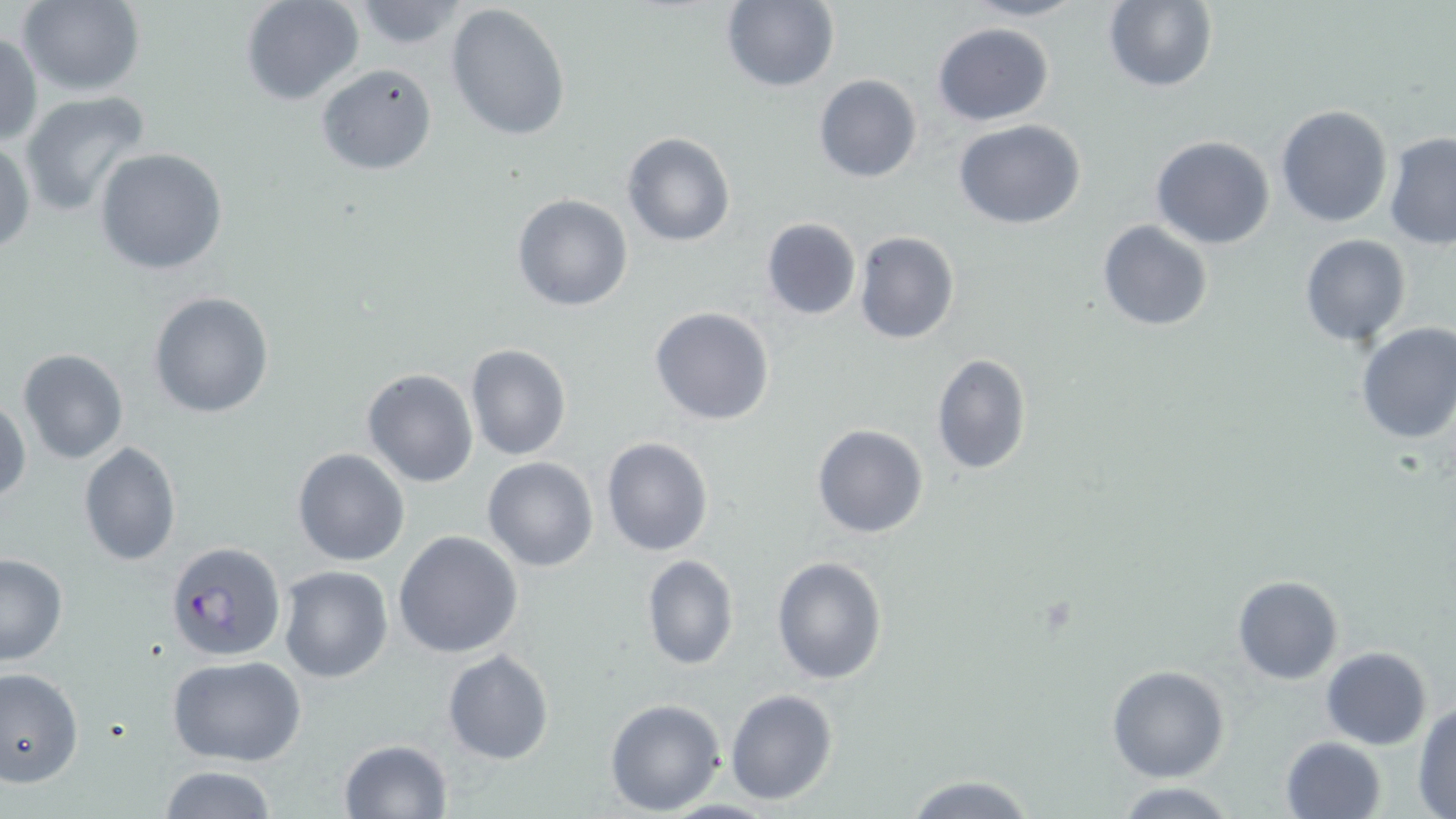
Summary:
  - Coordinate format: approximate bounding boxes as (x1,y1)-(x2,y2) corner pairs in pixels
  - Uninfected red blood cell locations: (240,0)-(364,106), (717,0)-(841,92), (964,0)-(1085,23), (16,1)-(147,96), (1102,1)-(1219,92), (349,2)-(471,52), (444,3)-(572,143), (932,21)-(1054,125), (0,32)-(42,147), (314,63)-(438,175), (812,73)-(923,183), (19,92)-(154,217), (1274,104)-(1394,228), (952,118)-(1087,230), (1382,129)-(1455,249), (622,132)-(735,247), (1150,135)-(1276,251), (0,139)-(36,257), (94,146)-(229,276), (511,193)-(633,313), (760,218)-(862,320), (1096,219)-(1213,333), (854,231)-(960,344), (1299,233)-(1411,347), (148,290)-(275,419), (649,306)-(777,425), (1354,321)-(1456,445), (466,344)-(571,460), (16,349)-(130,465), (930,353)-(1032,476), (361,367)-(479,488), (0,399)-(30,506), (811,423)-(928,539), (600,436)-(713,556), (78,442)-(182,566), (292,447)-(411,566), (482,457)-(598,572), (394,529)-(524,659), (0,554)-(69,667), (640,555)-(738,670), (771,555)-(888,685), (278,565)-(394,682), (1232,575)-(1344,684), (1321,647)-(1432,749), (442,649)-(555,764), (168,655)-(307,766), (0,665)-(84,789), (1107,665)-(1230,782), (725,688)-(840,805), (604,698)-(725,815), (1413,702)-(1456,816), (1279,736)-(1385,819), (338,739)-(452,818), (157,765)-(280,819), (902,774)-(1038,817), (1113,781)-(1242,817)
  - Plasmodium falciparum-infected red blood cell locations: (166,540)-(287,664)
  - Slide-level diagnosis: Plasmodium falciparum
  - Modality: light microscopy
  - Stain: May-Grünwald-Giemsa
  - Preparation: thin blood film
  - Magnification: 1000x
  - Field of view: one of a larger specimen
  - Image size: 1456×819 pixels